Report the malaria status of this cell.
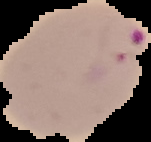
Parasitized.

image type = segmented cell region with the area outside set to black
image size = 151×142 pixels
preparation = thin blood film